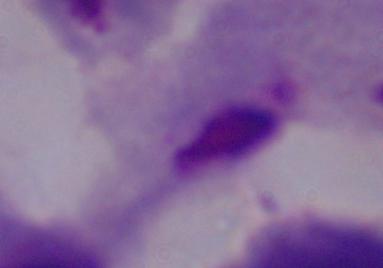

A trichomonad is shown. 1000x magnification. Photomicrograph.